Describe the morphology of the red blood cells.
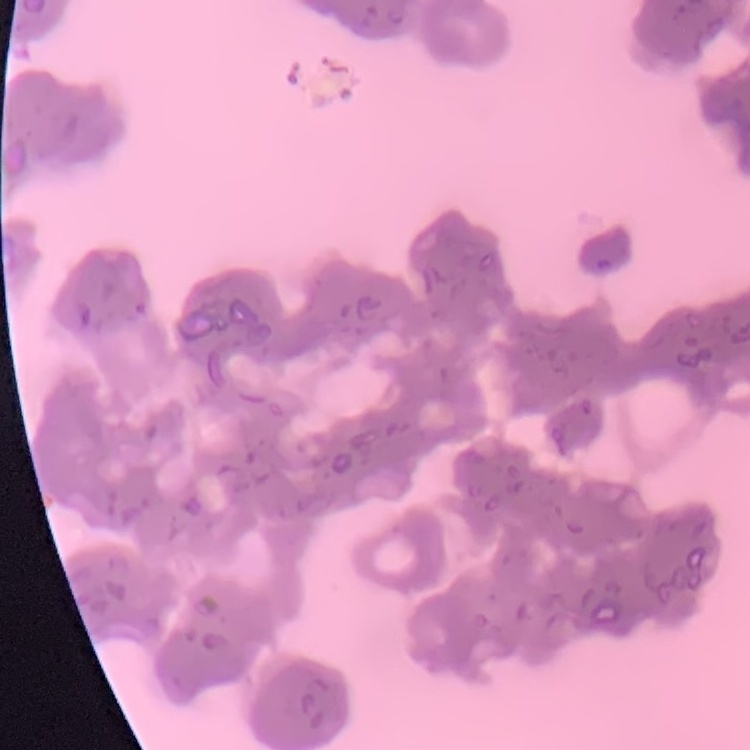
They show rouleaux formation.

image type = square crop of a larger photomicrograph
stain = Field's or Giemsa
preparation = thin blood film